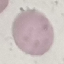

result: no malaria parasites seen
stain: Giemsa
preparation: thin blood smear
capture: smartphone through the microscope eyepiece
image_type: automatically extracted cell patch, resized to 64 × 64 pixels